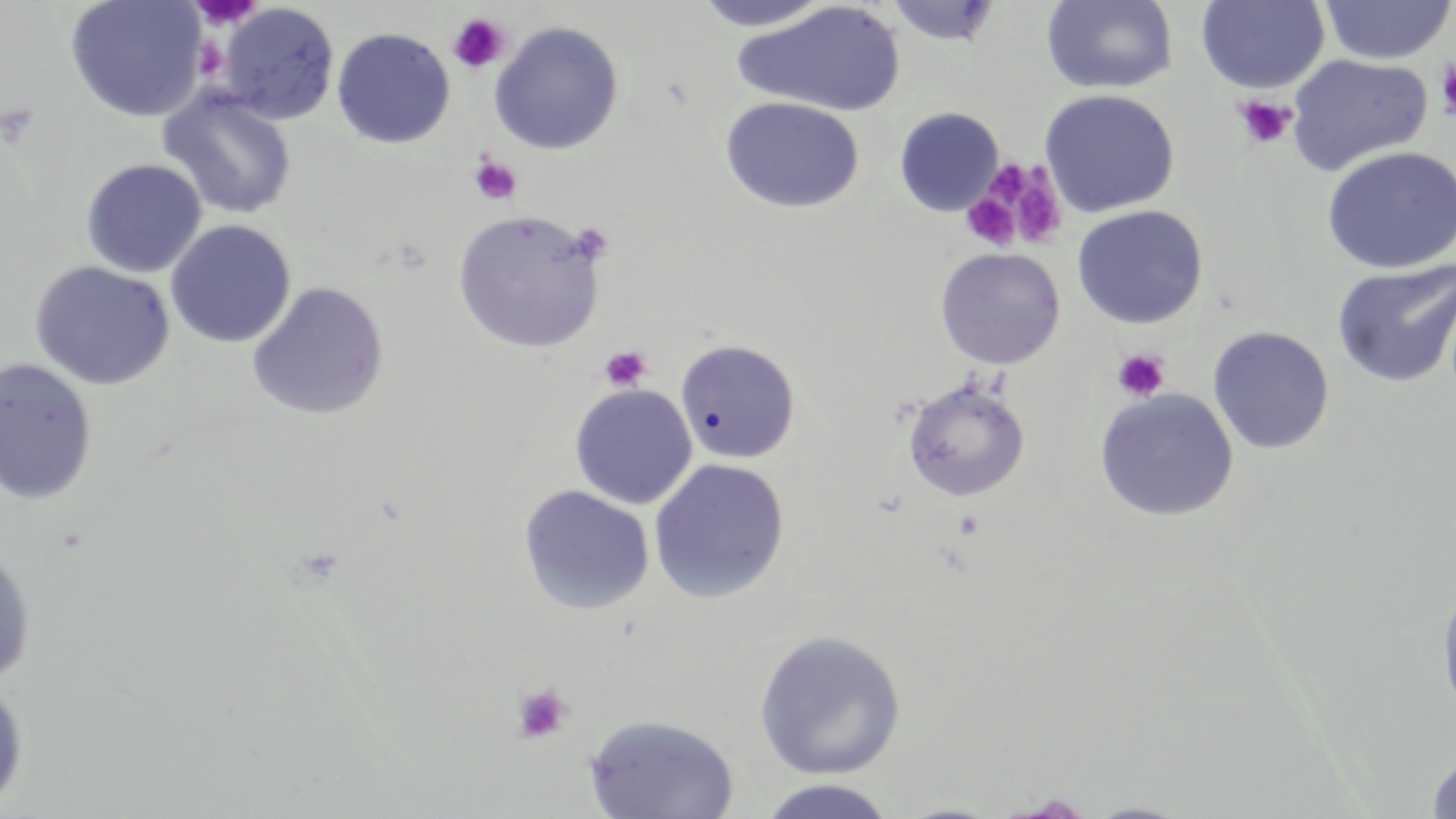

slide-level diagnosis = no evidence of blood parasites
image size = 1456×819 pixels
field of view = single
stain = May-Grünwald-Giemsa
preparation = thin blood film
uninfected red blood cell locations = approximate bounding boxes as (x1,y1)-(x2,y2) corner pairs in pixels: (66,0)-(208,122), (690,0)-(837,32), (1196,0)-(1329,93), (1318,0)-(1455,65), (733,1)-(906,118), (885,1)-(1002,47), (1041,1)-(1178,94), (217,3)-(339,125), (488,21)-(624,155), (331,27)-(455,149), (1285,53)-(1433,176), (158,88)-(297,220), (1038,89)-(1180,217), (719,96)-(864,214), (894,107)-(1004,216), (1321,145)-(1455,273), (80,159)-(207,278), (1071,204)-(1209,329), (452,210)-(605,352), (165,220)-(296,349), (934,247)-(1066,370), (1331,259)-(1456,389), (29,261)-(175,390), (247,282)-(389,421), (1208,326)-(1334,455), (674,339)-(801,464), (0,358)-(98,505), (901,377)-(1031,503), (568,384)-(697,510), (1094,388)-(1239,521), (648,458)-(790,603), (518,485)-(655,615), (0,546)-(36,686), (1436,576)-(1456,723), (753,630)-(906,779), (0,677)-(28,813), (583,714)-(739,819), (1424,746)-(1456,818), (755,779)-(902,819), (994,793)-(1099,818), (1080,799)-(1197,818)
magnification = 1000x
modality = light microscopy
platelet locations = approximate bounding boxes as (x1,y1)-(x2,y2) corner pairs in pixels: (188,0)-(263,30), (448,13)-(510,74), (1434,56)-(1456,122), (1234,95)-(1295,151), (468,154)-(522,206), (997,165)-(1067,250), (961,193)-(1020,250), (598,345)-(652,391), (1111,348)-(1170,402), (510,684)-(573,745)